Locate the red blood cells and classify each one as P. falciparum-infected, uninfected, or of indeterminate infection status.
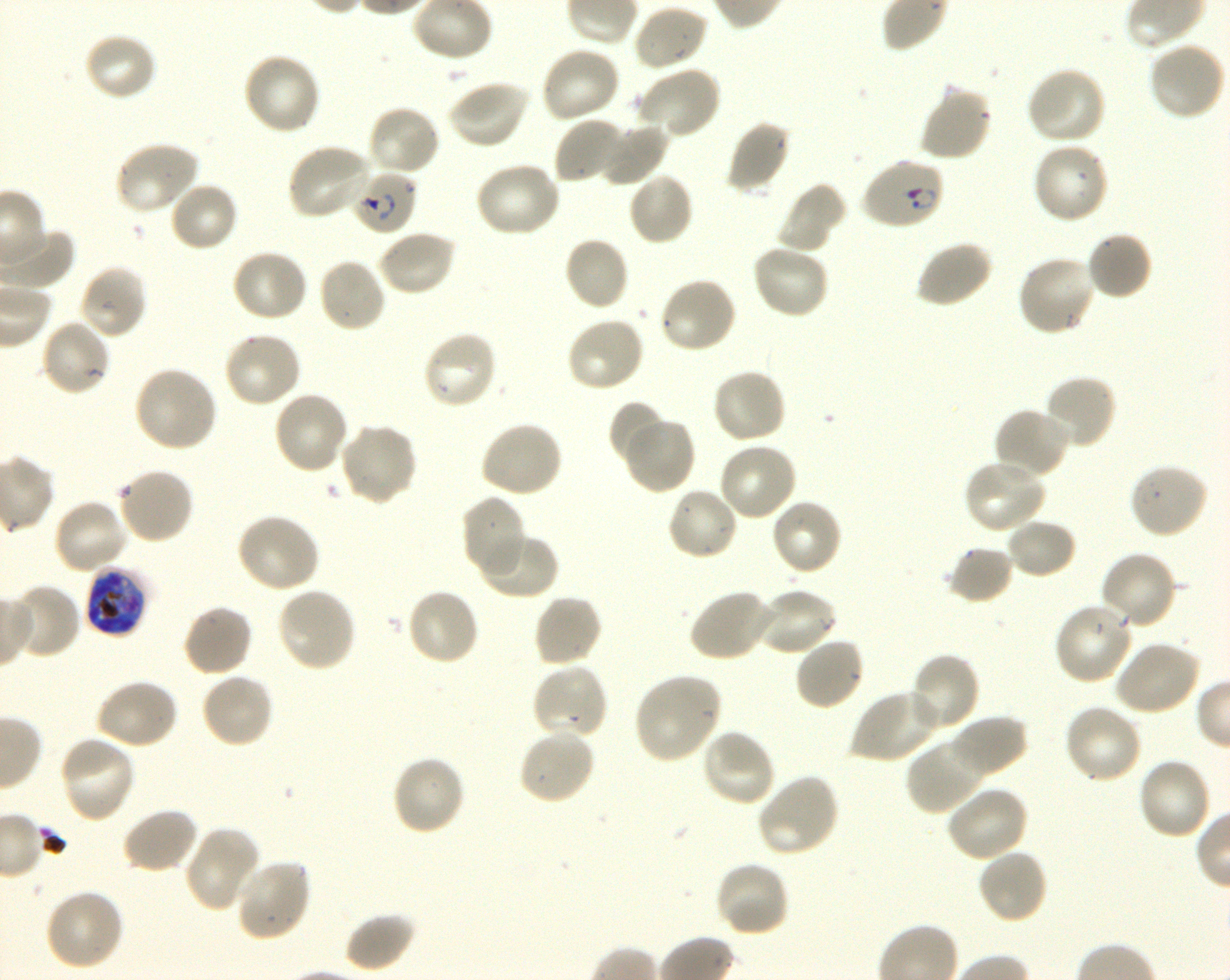

Approximate bounding boxes as (x1, y1, x2, y2) in pixels. Not every red blood cell is marked. A life-cycle stage — or a range of stages, where the recorded stages span more than one — follows each staged infected red blood cell.
Infected red blood cells: (860, 157, 946, 230) ring; (351, 169, 418, 235) ring; (85, 563, 147, 636) late trophozoite to late schizont.
Uninfected red blood cells: (632, 4, 709, 72), (83, 32, 159, 102), (1148, 42, 1226, 122), (540, 44, 621, 123), (242, 51, 322, 136), (636, 65, 722, 140), (1024, 66, 1106, 146), (446, 79, 531, 149), (918, 83, 994, 162), (366, 105, 442, 178), (552, 116, 627, 186), (728, 118, 791, 196), (596, 120, 669, 187), (113, 141, 201, 215), (1032, 141, 1110, 225), (285, 143, 374, 221), (474, 161, 561, 238), (627, 171, 694, 246), (168, 181, 239, 253), (775, 182, 847, 254), (377, 229, 457, 296), (1085, 230, 1154, 301), (563, 235, 630, 312), (915, 239, 993, 309), (751, 243, 830, 319), (231, 248, 309, 323), (1016, 255, 1098, 337), (317, 258, 387, 334), (79, 264, 148, 340), (658, 277, 738, 355), (565, 316, 646, 393), (39, 317, 112, 397), (223, 329, 302, 409), (422, 329, 498, 410), (133, 364, 219, 454), (711, 367, 788, 445), (1043, 374, 1118, 451), (272, 389, 350, 475), (608, 400, 666, 466), (993, 406, 1070, 480), (622, 416, 697, 494), (479, 420, 564, 499), (337, 423, 418, 507), (718, 441, 799, 523), (962, 458, 1048, 533), (1129, 462, 1209, 540), (117, 465, 195, 545), (665, 486, 740, 562), (462, 494, 529, 579), (53, 498, 130, 574), (771, 498, 844, 575), (235, 512, 321, 593), (1004, 517, 1078, 579), (477, 532, 558, 600), (946, 545, 1015, 605), (1099, 551, 1178, 630), (8, 583, 81, 659), (276, 587, 357, 673), (405, 587, 481, 667), (756, 587, 838, 656), (688, 588, 774, 663), (532, 593, 604, 668), (1053, 601, 1135, 685), (181, 603, 254, 677), (793, 635, 865, 711), (1111, 640, 1202, 717), (908, 651, 980, 731), (531, 662, 610, 740), (200, 672, 276, 749), (633, 673, 723, 763), (95, 678, 180, 750), (850, 688, 943, 764), (1063, 702, 1143, 785), (948, 714, 1028, 779), (518, 728, 595, 806), (699, 728, 777, 808), (58, 735, 137, 824), (906, 736, 988, 815), (390, 754, 466, 836), (1136, 756, 1212, 841), (756, 773, 842, 858), (944, 786, 1028, 862), (122, 807, 200, 875), (184, 828, 260, 912), (976, 848, 1049, 925), (234, 858, 312, 942), (714, 859, 790, 938), (42, 888, 125, 971), (344, 912, 417, 972).
No red blood cells of indeterminate infection status observed.

Summary:
  - Objective: 100x, oil immersion, numerical aperture 1.30
  - Image size: 1230×980 pixels
  - Donor blood group: O+
  - Culture: shaking in-vitro P. falciparum strain 3D7
  - Stain: Giemsa
  - Field of view: single
  - Preparation: thin blood film